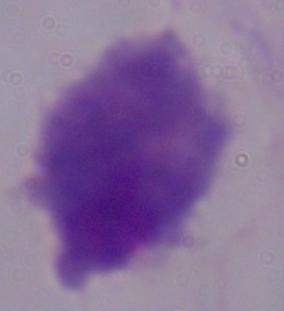

Summary:
  - Identification: trichomonad
  - Magnification: 1000x
  - Modality: micrograph